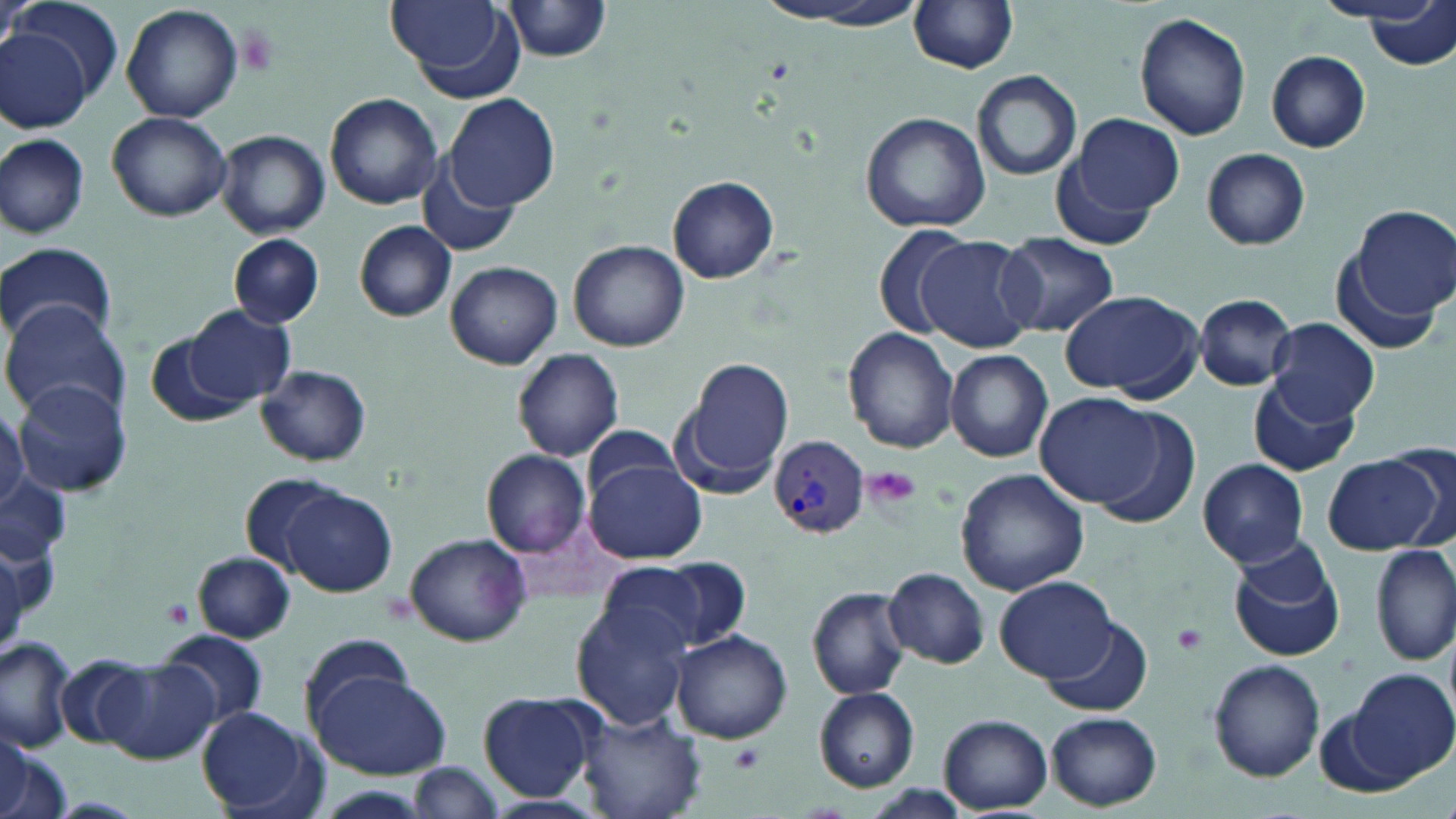
{
  "plasmodium_vivax_infected_red_blood_cell_locations": "approximate bounding boxes as (x1, y1, x2, y2) in pixels: (769, 437, 869, 537)",
  "slide_level_diagnosis": "Plasmodium vivax",
  "preparation": "thin blood smear",
  "magnification": "1000x",
  "image_size": "1456×819 pixels",
  "platelet_locations": "approximate bounding boxes as (x1, y1, x2, y2) in pixels: (862, 465, 923, 512), (161, 597, 194, 630), (1171, 623, 1208, 656), (730, 743, 767, 773)",
  "uninfected_red_blood_cell_locations": "approximate bounding boxes as (x1, y1, x2, y2) in pixels: (10, 0, 124, 106), (384, 0, 520, 97), (1314, 0, 1443, 26), (501, 1, 615, 60), (755, 1, 932, 31), (910, 1, 1021, 74), (121, 3, 244, 123), (1365, 3, 1453, 70), (1133, 11, 1252, 141), (0, 30, 90, 131), (1265, 50, 1371, 152), (970, 70, 1082, 181), (324, 92, 444, 210), (447, 94, 558, 213), (107, 110, 233, 221), (859, 111, 990, 233), (1061, 112, 1185, 227), (216, 130, 331, 239), (0, 134, 90, 239), (1201, 147, 1310, 250), (419, 154, 520, 257), (667, 175, 779, 283), (1348, 205, 1456, 329), (353, 221, 458, 322), (871, 223, 977, 338), (995, 231, 1118, 337), (229, 234, 323, 328), (914, 236, 1038, 352), (0, 240, 116, 347), (569, 240, 690, 350), (445, 259, 563, 369), (1058, 288, 1207, 402), (1193, 293, 1298, 391), (1, 300, 132, 422), (185, 304, 294, 408), (1265, 317, 1380, 425), (842, 327, 959, 452), (147, 334, 254, 430), (512, 347, 625, 463), (945, 350, 1053, 461), (676, 357, 796, 492), (257, 364, 372, 467), (1247, 376, 1359, 475), (12, 380, 135, 496), (1036, 393, 1170, 508), (0, 403, 29, 514), (1087, 406, 1204, 529), (1388, 440, 1456, 551), (483, 449, 590, 558), (1322, 453, 1443, 554), (1197, 458, 1310, 567), (585, 460, 706, 563), (955, 468, 1090, 595), (239, 472, 344, 574), (278, 486, 398, 597), (404, 534, 532, 646), (1227, 542, 1346, 662), (1373, 542, 1455, 665), (192, 552, 296, 644), (600, 557, 745, 656), (883, 567, 990, 668), (994, 575, 1121, 684), (807, 585, 911, 700), (570, 603, 691, 728), (1040, 615, 1153, 716), (156, 629, 269, 731), (671, 630, 792, 744), (299, 633, 418, 728), (0, 635, 78, 750), (58, 655, 147, 749), (96, 659, 218, 765), (1209, 659, 1325, 781), (309, 668, 449, 778), (1347, 671, 1454, 784), (814, 687, 920, 792), (477, 691, 600, 802), (1317, 694, 1426, 797), (197, 706, 319, 815), (578, 708, 707, 819), (1046, 711, 1162, 811), (939, 714, 1052, 813), (0, 728, 29, 818), (0, 736, 59, 819), (406, 763, 508, 818), (476, 794, 608, 818)",
  "field_of_view": "one of a larger specimen",
  "modality": "optical microscopy",
  "stain": "May-Grünwald-Giemsa"
}